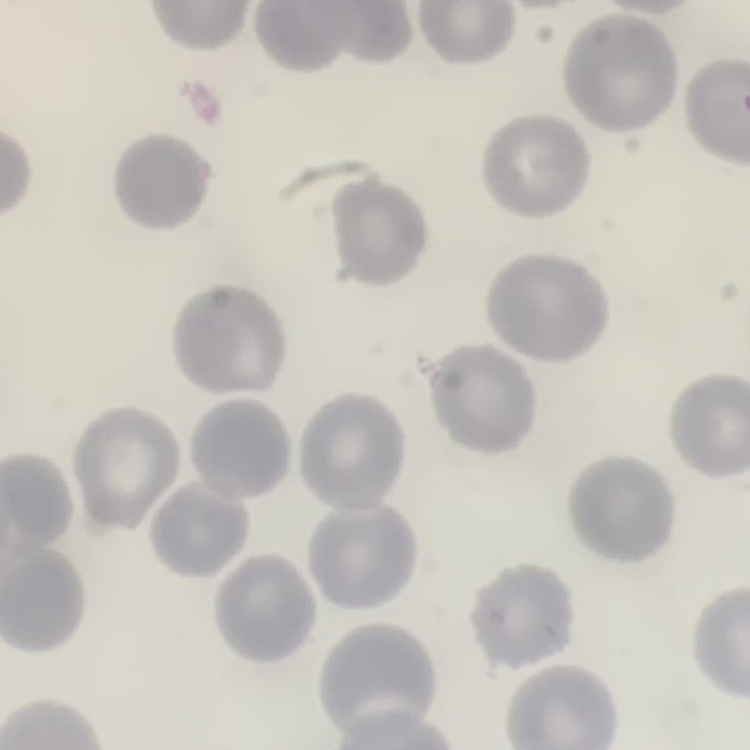

Summary:
  - Red blood cell morphology: no rouleaux formation
  - Image type: square crop of a larger photomicrograph
  - Preparation: thin peripheral smear
  - Stain: Field's or Giemsa